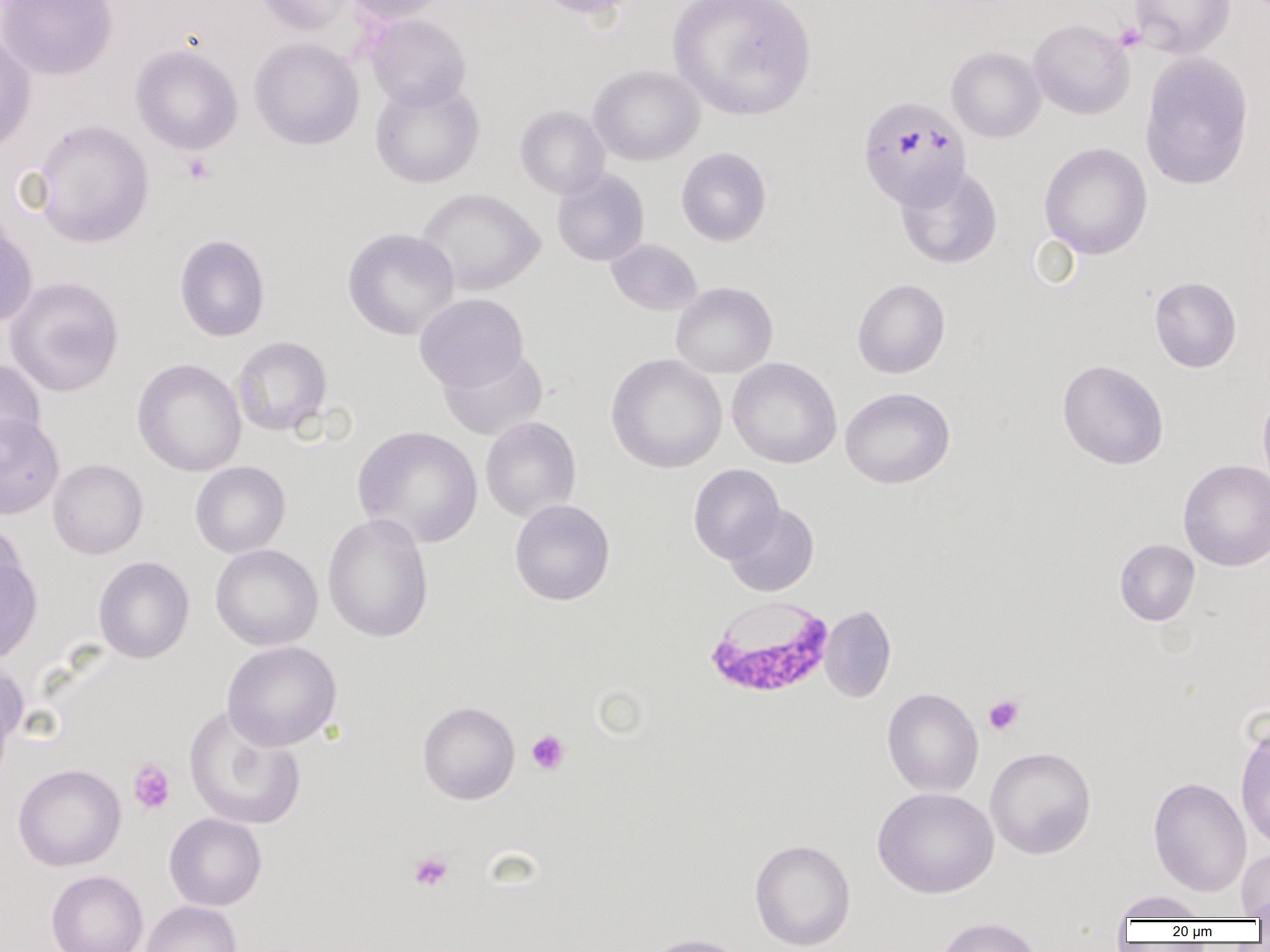
slide-level diagnosis = Plasmodium falciparum
magnification = 1000x
preparation = thin blood film
Plasmodium falciparum-infected red blood cell locations = approximate bounding boxes as (x1, y1, x2, y2) in pixels: (704, 596, 834, 698)
image size = 1270×952 pixels
modality = light microscopy
uninfected red blood cell locations = approximate bounding boxes as (x1, y1, x2, y2) in pixels: (0, 0, 118, 81), (255, 0, 356, 36), (343, 0, 451, 23), (530, 0, 648, 20), (668, 0, 816, 121), (1130, 0, 1235, 59), (364, 13, 472, 111), (1028, 18, 1135, 119), (0, 32, 37, 154), (249, 37, 364, 150), (130, 43, 243, 155), (946, 46, 1046, 143), (1139, 52, 1254, 191), (588, 64, 705, 166), (370, 77, 485, 189), (857, 94, 971, 212), (515, 105, 610, 199), (32, 119, 154, 248), (1039, 142, 1152, 259), (676, 147, 772, 247), (895, 165, 1002, 269), (552, 168, 649, 267), (416, 187, 544, 296), (0, 215, 38, 328), (342, 227, 460, 341), (174, 233, 271, 342), (606, 238, 702, 315), (5, 276, 125, 397), (1149, 276, 1241, 373), (852, 278, 950, 379), (671, 282, 778, 378), (415, 294, 529, 393), (232, 336, 332, 436), (438, 347, 548, 441), (606, 354, 727, 473), (727, 357, 841, 468), (132, 358, 247, 477), (1057, 359, 1169, 469), (0, 360, 47, 459), (840, 387, 955, 489), (1258, 392, 1270, 490), (0, 412, 65, 519), (480, 416, 581, 522), (352, 425, 482, 548), (47, 458, 148, 559), (1178, 459, 1270, 572), (190, 461, 290, 558), (688, 464, 784, 564), (510, 499, 615, 606), (724, 503, 819, 597), (322, 513, 433, 642), (0, 518, 27, 608), (1114, 539, 1200, 626), (210, 544, 323, 651), (0, 552, 43, 666), (93, 556, 194, 664), (820, 605, 896, 703), (222, 641, 342, 750), (0, 661, 28, 769), (882, 687, 984, 798), (418, 701, 520, 804), (183, 704, 305, 831), (1235, 723, 1270, 851), (985, 746, 1096, 860), (13, 763, 126, 871), (1148, 776, 1251, 897), (873, 787, 999, 898), (164, 812, 267, 911), (749, 838, 856, 951), (1236, 848, 1270, 920), (46, 870, 148, 952), (1112, 890, 1211, 922), (140, 900, 242, 952), (932, 915, 1045, 952), (638, 933, 752, 952)
field of view = one of a larger specimen
platelet locations = approximate bounding boxes as (x1, y1, x2, y2) in pixels: (1114, 22, 1145, 51), (182, 154, 216, 184), (983, 695, 1024, 735), (526, 730, 570, 775), (128, 759, 175, 814), (408, 850, 454, 891)